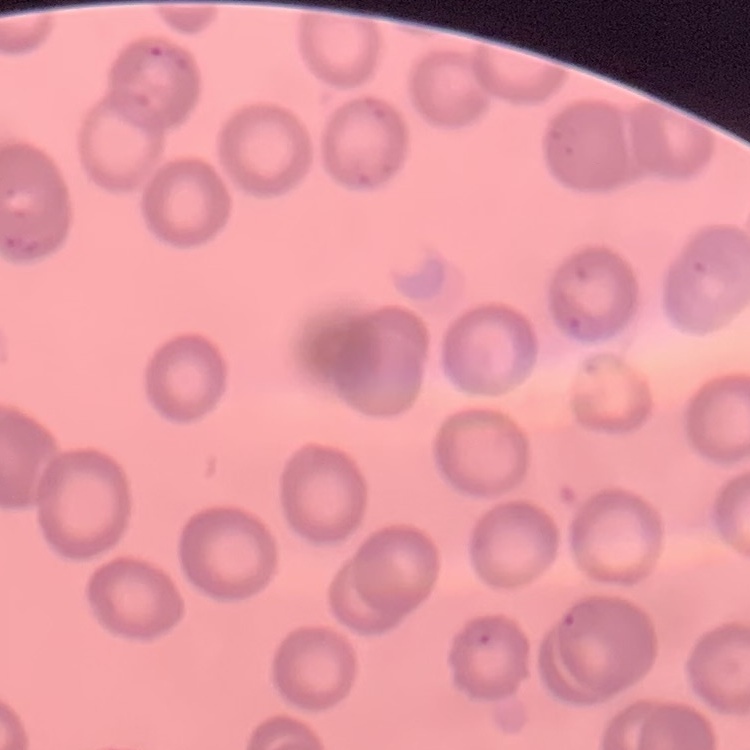
Summary:
  - Erythrocyte morphology: no rouleaux formation
  - Preparation: thin peripheral smear
  - Image type: one tile cut from a larger photomicrograph
  - Stain: Field's or Giemsa